Classify this cell by malaria status.
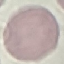

Uninfected.

Summary:
  - Image type: automatically extracted cell patch, resized to 64 × 64 pixels
  - Capture: smartphone through the microscope eyepiece
  - Stain: Giemsa
  - Preparation: thin smear